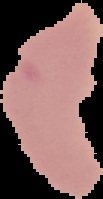

Malaria status: uninfected. Image is 103×199 pixels. Cell region segmented out of the field of view; the surrounding area is masked to black. From a thin blood film.